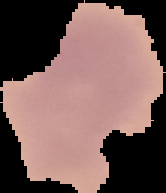
Summary:
  - Image size: 166×193 pixels
  - Image type: cell region segmented out of the field of view; surrounding area masked to black
  - Preparation: thin blood smear
  - Result: no Plasmodium parasites seen